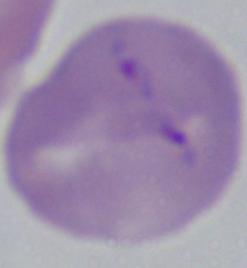
modality = photomicrograph
identification = Babesia
magnification = 1000x